Point out each malaria parasite.
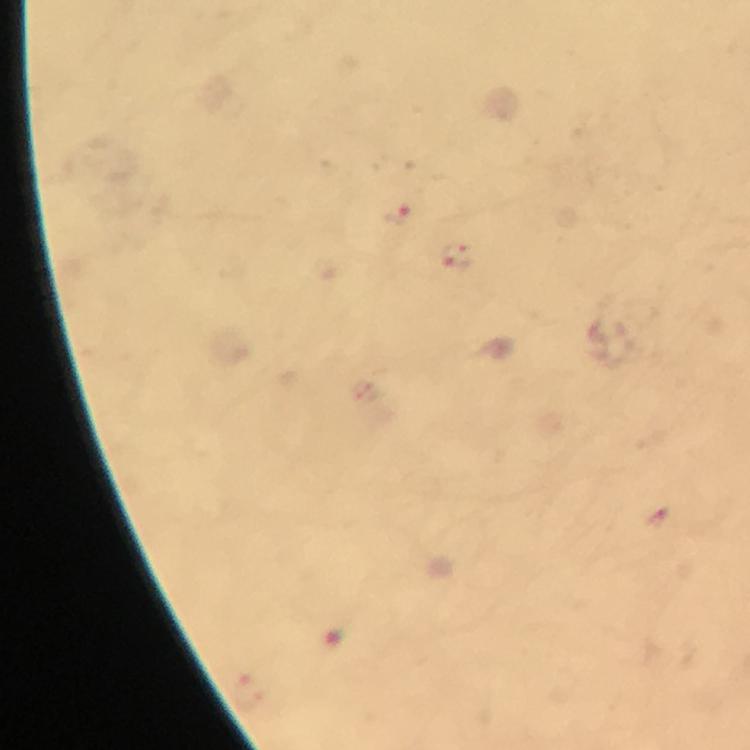
Approximate centers as (x, y) in pixels.
Malaria parasites: (396, 213), (456, 256).

Cropped region of a single field of view. Thick blood film. Immersion oil applied. 100x magnification. Image is 750×750 pixels. Photographed through the microscope with a smartphone camera. From a diagnostic examination for malaria. Giemsa-stained preparation.